Classify this cell by malaria status.
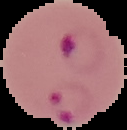

Parasitized.

image size = 127×130 pixels
image type = segmented cell region with the area outside set to black
preparation = thin blood film